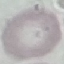 Result: no malaria parasites detected. Thin blood film. Giemsa-stained preparation. Cell patch, automatically extracted from a larger field of view and resized to 64 × 64 pixels. Acquired by smartphone through the microscope eyepiece.